Locate the cells, classifying each as a parasitized red blood cell, an uninfected red blood cell, or a white blood cell.
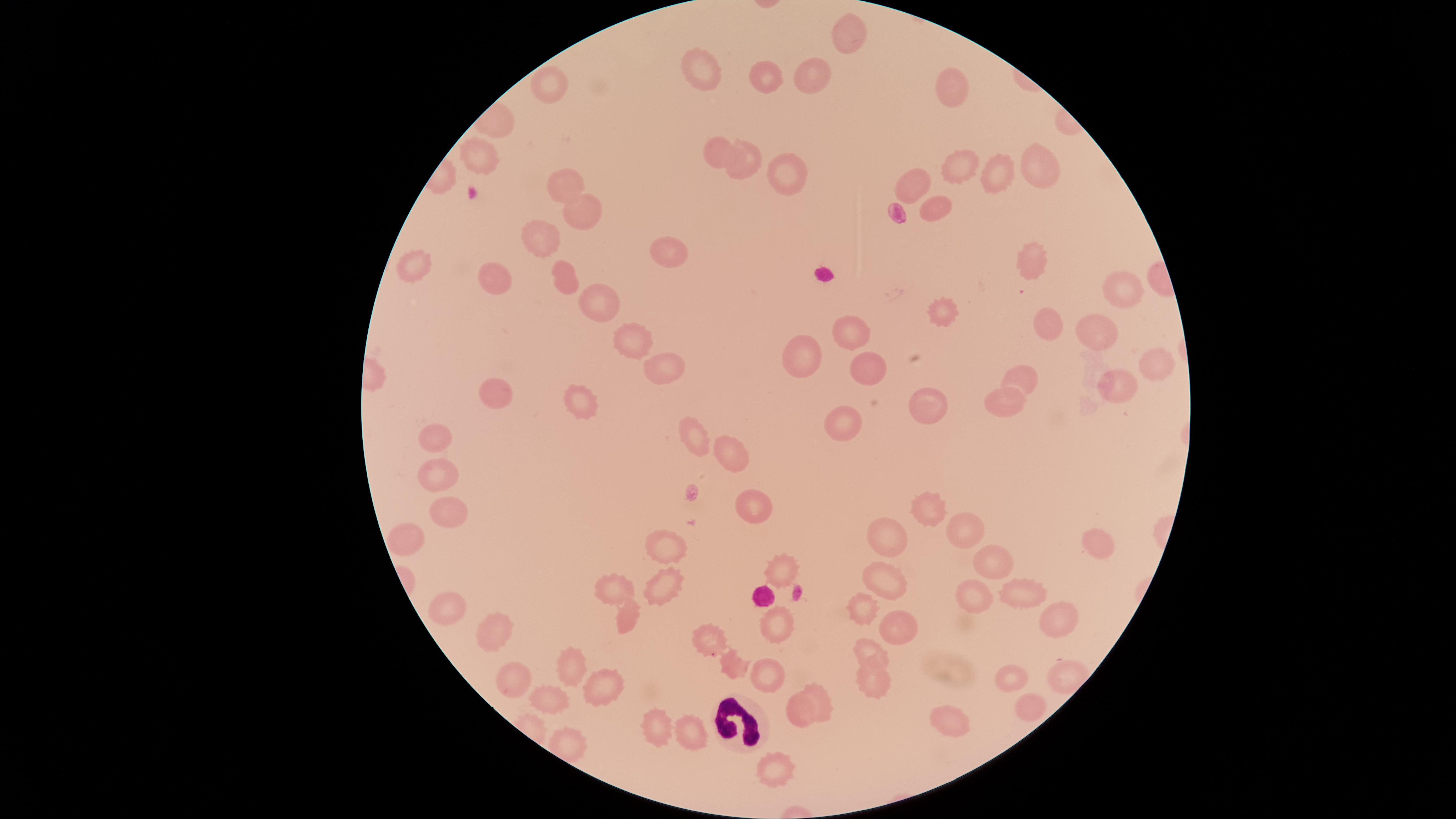

No parasitized red blood cells identified.
Approximate marker points as [x, y] in pixels.
Uninfected red blood cells: [844, 36], [701, 69], [808, 75], [765, 78], [547, 89], [949, 89], [717, 154], [1039, 159], [745, 161], [479, 165], [959, 168], [782, 172], [990, 174], [563, 180], [915, 180], [938, 207], [579, 213], [542, 240], [669, 254], [1034, 264], [417, 265], [499, 276], [559, 278], [1119, 289], [595, 307], [947, 310], [1052, 323], [1097, 325], [850, 329], [635, 334], [803, 354], [1151, 362], [867, 363], [660, 371], [1024, 378], [1110, 382], [496, 390], [579, 400], [1005, 401], [927, 404], [843, 420], [433, 434], [695, 435], [731, 463], [434, 475], [750, 509], [928, 510], [445, 518], [962, 530], [882, 534], [403, 536], [662, 541], [1095, 543], [778, 567], [985, 567], [880, 580], [662, 582], [612, 591], [1024, 595], [970, 602], [451, 606], [863, 606], [1059, 615], [624, 618], [499, 629], [776, 629], [895, 641], [713, 643], [874, 650], [574, 660], [735, 662], [765, 672], [1007, 674], [517, 678], [872, 680], [603, 683], [549, 696], [818, 707], [797, 709], [1025, 712], [950, 718], [690, 727], [656, 728], [776, 767].
White blood cells: [739, 721].

Smartphone photograph through the microscope eyepiece. One field of view of the specimen. Circular visible region. Image is 1456×819 pixels. Thin blood film. Giemsa stain.